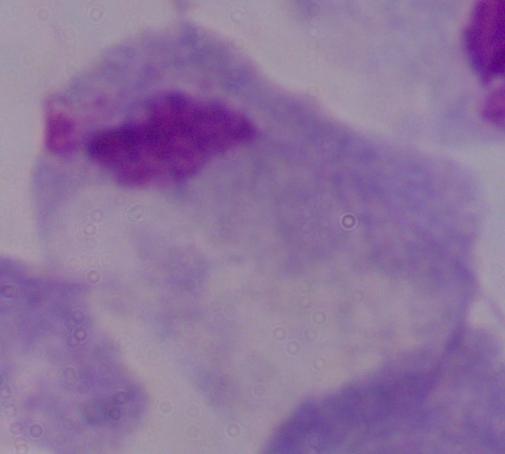
Photomicrograph. A trichomonad is shown. 1000x magnification.